Assess this cell for malaria.
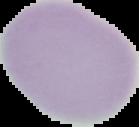

It is uninfected.

Summary:
  - Preparation: thin blood film
  - Image type: cell region segmented out of the field of view; surrounding area masked to black
  - Image size: 139×127 pixels